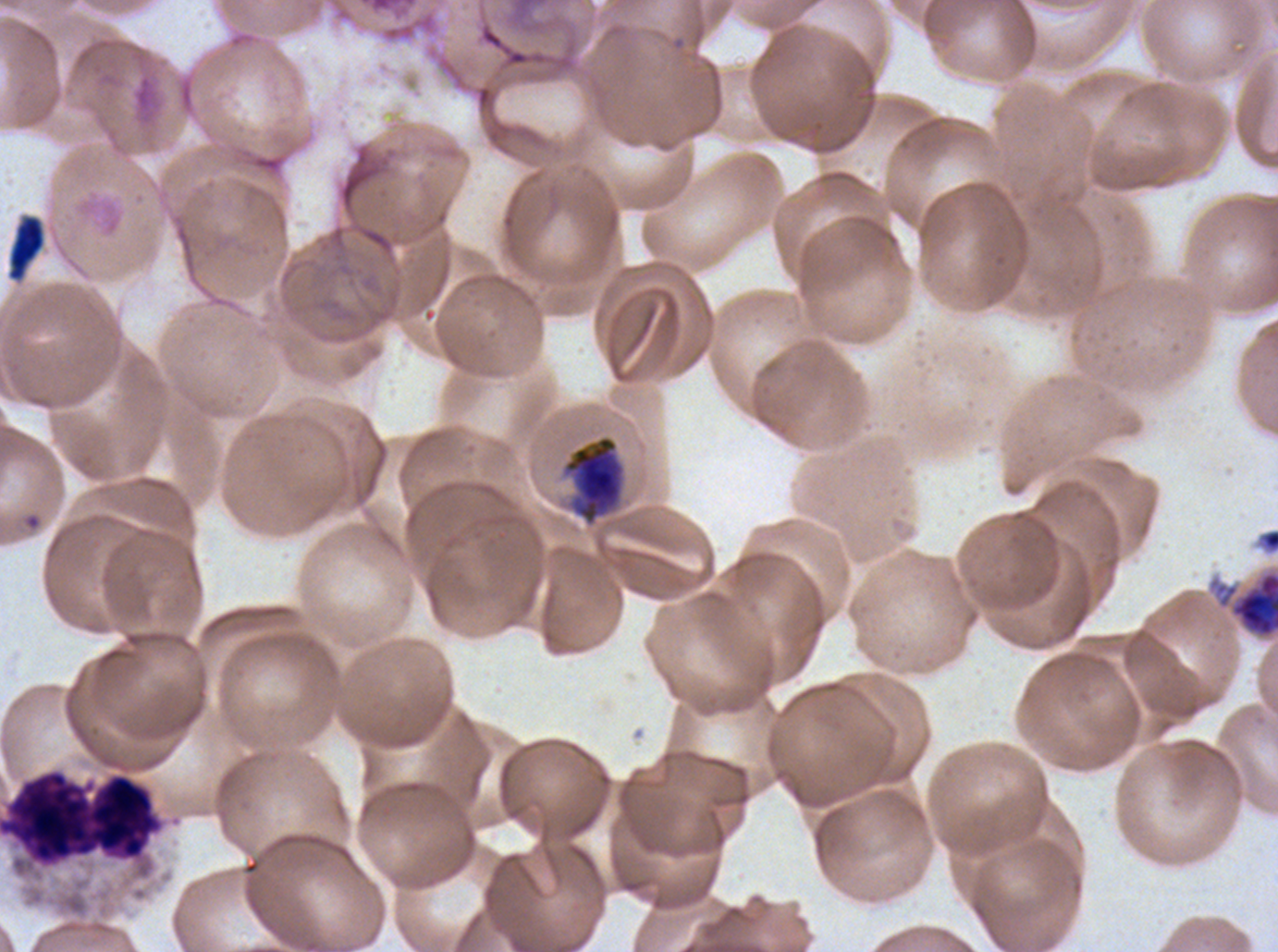

field_of_view: sub-image separated from a larger composite
image_size: 1278×952 pixels
preparation: thin blood smear
leukocyte_locations: 'approximate bounding boxes as (x1, y1, x2, y2) in pixels: (0, 768, 165, 868)'
early_schizont_locations: 'approximate bounding boxes as (x1, y1, x2, y2) in pixels: (1231, 571, 1277, 638)'
late_schizont_locations: 'approximate bounding boxes as (x1, y1, x2, y2) in pixels: (564, 435, 622, 522)'
specimen: P. falciparum from a patient in The Gambia, cultured ex vivo for 24 to 48 hours
stain: Giemsa
debris_locations: 'approximate bounding boxes as (x1, y1, x2, y2) in pixels: (7, 214, 45, 282)'
life_cycle_stages_observed: early schizont, late schizont